Point out every Plasmodium parasite and every leukocyte.
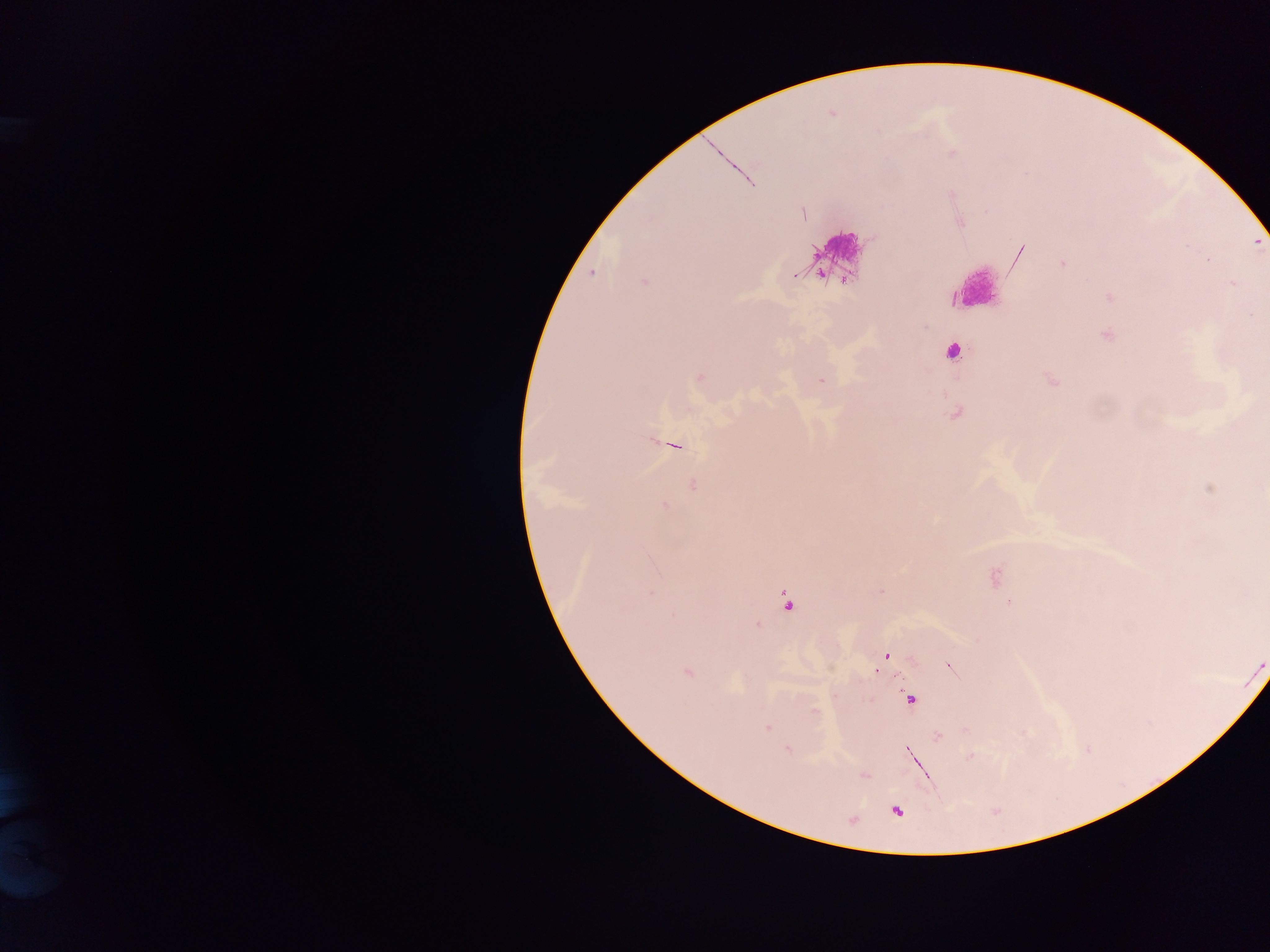

Approximate centers as {x, y} in pixels.
Plasmodium parasites: {952, 152}, {803, 212}, {1062, 264}, {592, 273}, {644, 282}, {953, 352}, {700, 377}, {821, 380}, {674, 445}, {693, 485}, {664, 507}, {996, 577}, {651, 594}, {787, 601}, {1009, 603}, {757, 625}, {886, 657}, {950, 666}, {687, 673}, {910, 699}, {815, 711}, {768, 727}, {938, 736}, {788, 749}, {913, 756}, {970, 756}, {864, 775}, {896, 811}.
Leukocytes: {838, 246}, {979, 286}.

Mobile-phone photograph taken through the microscope. Thick blood smear. Image is 1270×952 pixels. Sample from Ghana. One field of view.